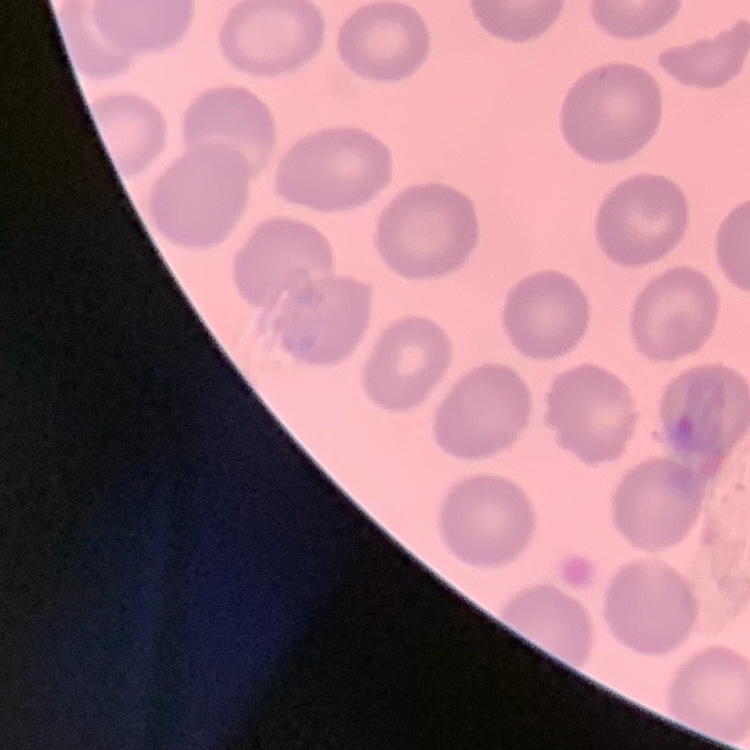 The erythrocytes exhibit no rouleaux formation. Field's or Giemsa stain. One tile cut from a larger photomicrograph. Thin blood smear.